Describe the morphology of the red blood cells.
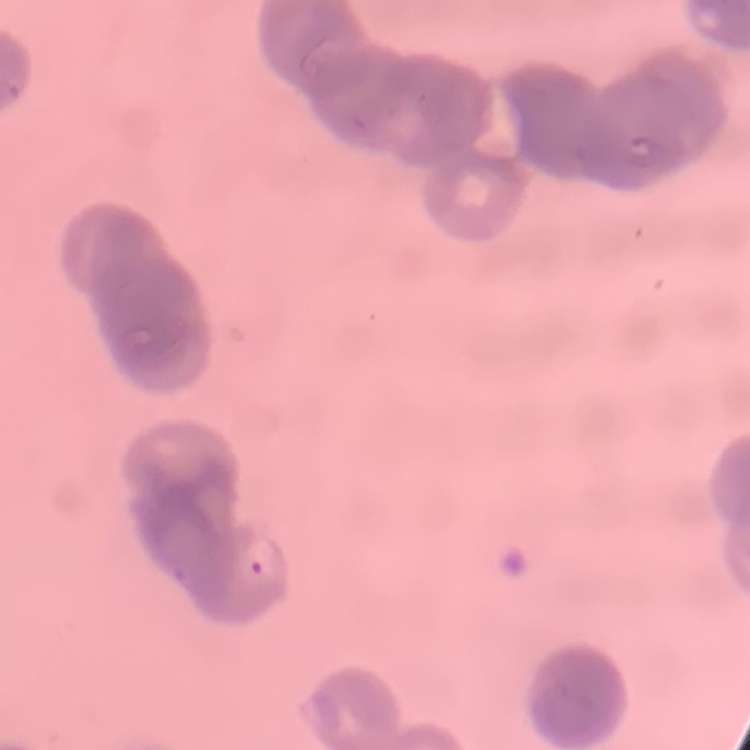

They show rouleaux formation.

Summary:
  - Stain: Field's or Giemsa
  - Image type: one tile cut from a larger photomicrograph
  - Preparation: thin blood film